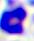

Summary:
  - Magnification: 400x
  - Modality: micrograph
  - Identification: leukocyte